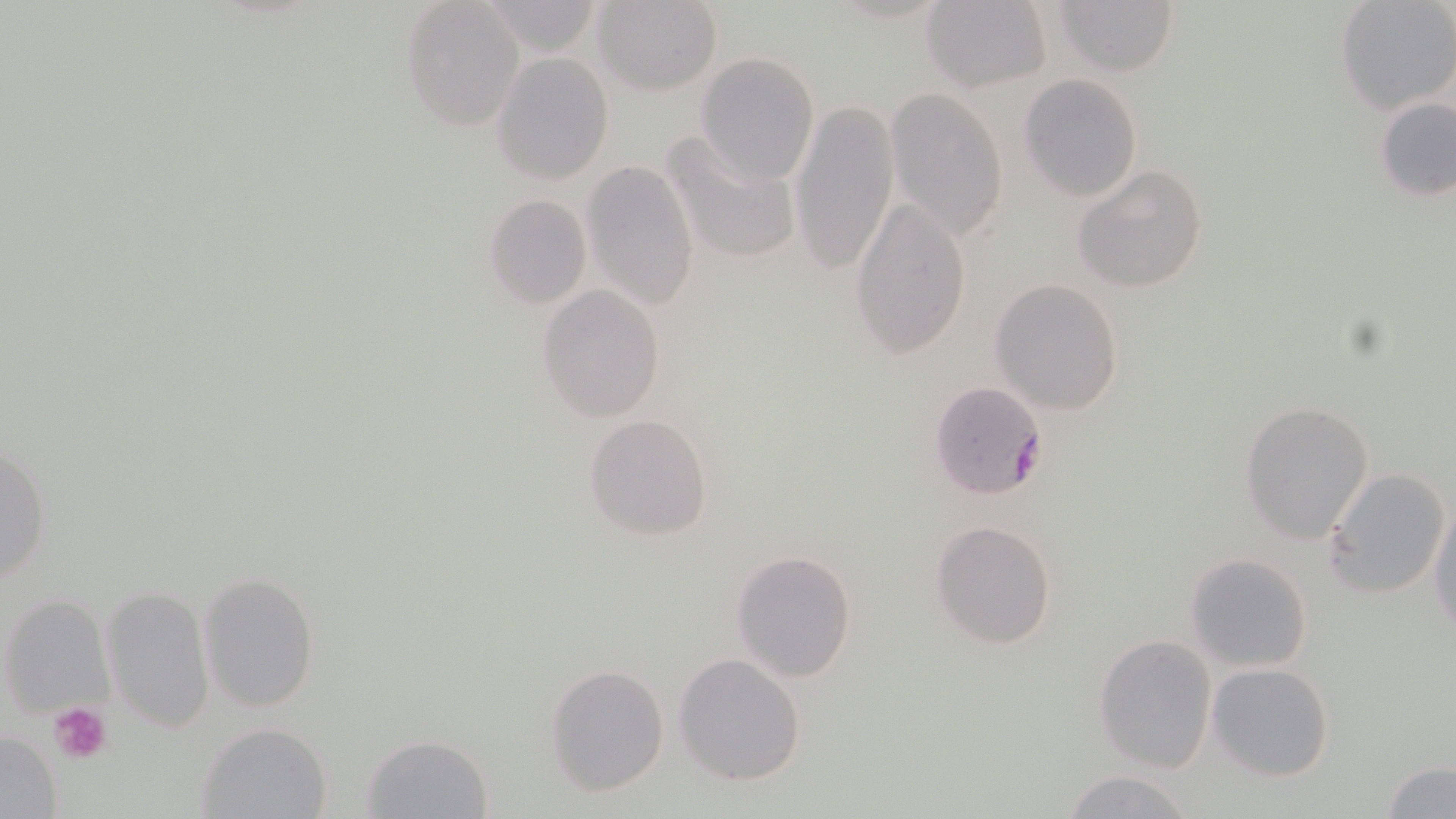
{
  "slide_level_diagnosis": "Plasmodium falciparum",
  "platelet_locations": "approximate bounding boxes as [x1, y1, x2, y2] in pixels: [48, 702, 112, 762]",
  "image_size": "1456×819 pixels",
  "stain": "May-Grünwald-Giemsa",
  "field_of_view": "single",
  "uninfected_red_blood_cell_locations": "approximate bounding boxes as [x1, y1, x2, y2] in pixels: [593, 0, 722, 96], [919, 0, 1052, 93], [1052, 0, 1179, 77], [1336, 0, 1456, 115], [480, 1, 605, 58], [399, 2, 523, 131], [491, 52, 614, 185], [695, 52, 821, 184], [1019, 73, 1144, 200], [883, 87, 1010, 243], [792, 95, 900, 277], [1375, 95, 1456, 201], [659, 128, 804, 268], [582, 160, 701, 311], [1072, 164, 1210, 293], [850, 193, 975, 361], [483, 194, 591, 309], [991, 277, 1124, 415], [537, 285, 667, 424], [1240, 401, 1375, 543], [583, 414, 714, 542], [1, 441, 52, 589], [1324, 465, 1452, 599], [1429, 494, 1456, 634], [930, 520, 1058, 651], [731, 549, 857, 683], [1185, 553, 1314, 673], [197, 570, 323, 714], [102, 582, 213, 732], [4, 593, 115, 719], [1095, 634, 1218, 772], [674, 652, 807, 785], [1206, 662, 1334, 782], [545, 663, 669, 796], [194, 720, 332, 817], [0, 730, 62, 816], [360, 732, 493, 817], [1383, 761, 1456, 818], [1061, 769, 1196, 819]",
  "preparation": "thin blood film",
  "magnification": "1000x",
  "modality": "optical microscopy",
  "plasmodium_falciparum_infected_red_blood_cell_locations": "approximate bounding boxes as [x1, y1, x2, y2] in pixels: [929, 380, 1050, 502]"
}